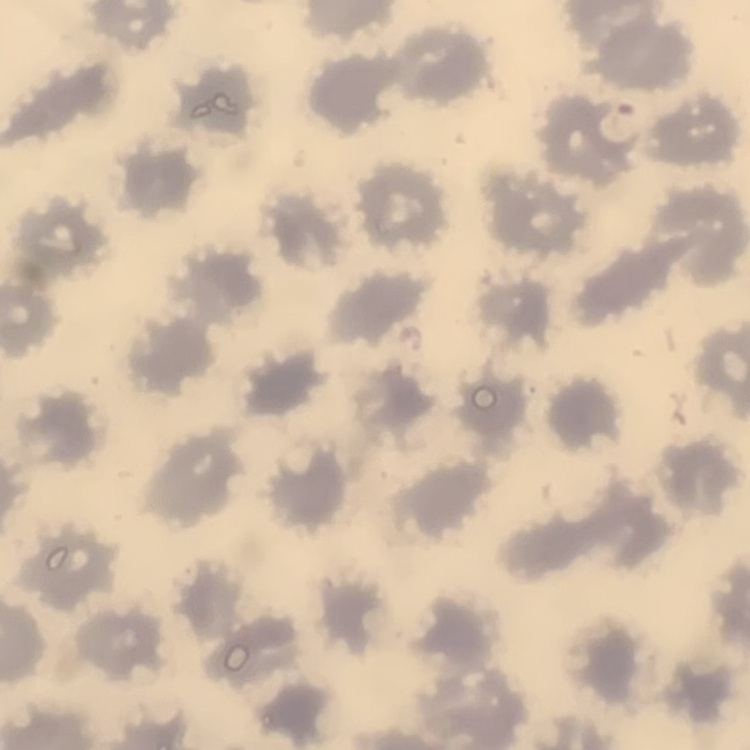

The erythrocytes exhibit no rouleaux formation. One tile cut from a larger photomicrograph. Stained with either Field's or Giemsa. Thin peripheral smear.